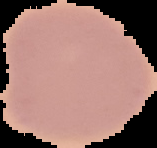

From a thin blood film. Image is 157×148 pixels. Cell region segmented out of the field of view; the surrounding area is masked to black. Result: no Plasmodium parasites detected.